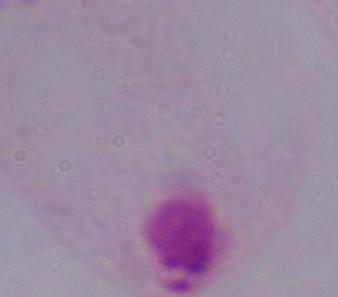
Summary:
  - Magnification: 1000x
  - Identification: trichomonad
  - Modality: micrograph